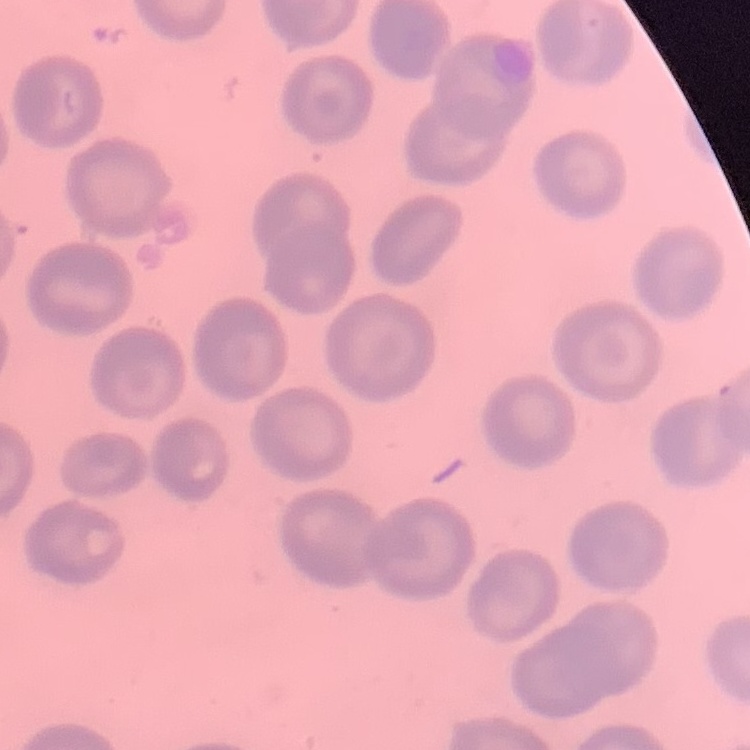

red_blood_cell_morphology: no rouleaux formation
image_type: square crop of a larger photomicrograph
preparation: thin blood smear
stain: Field's or Giemsa